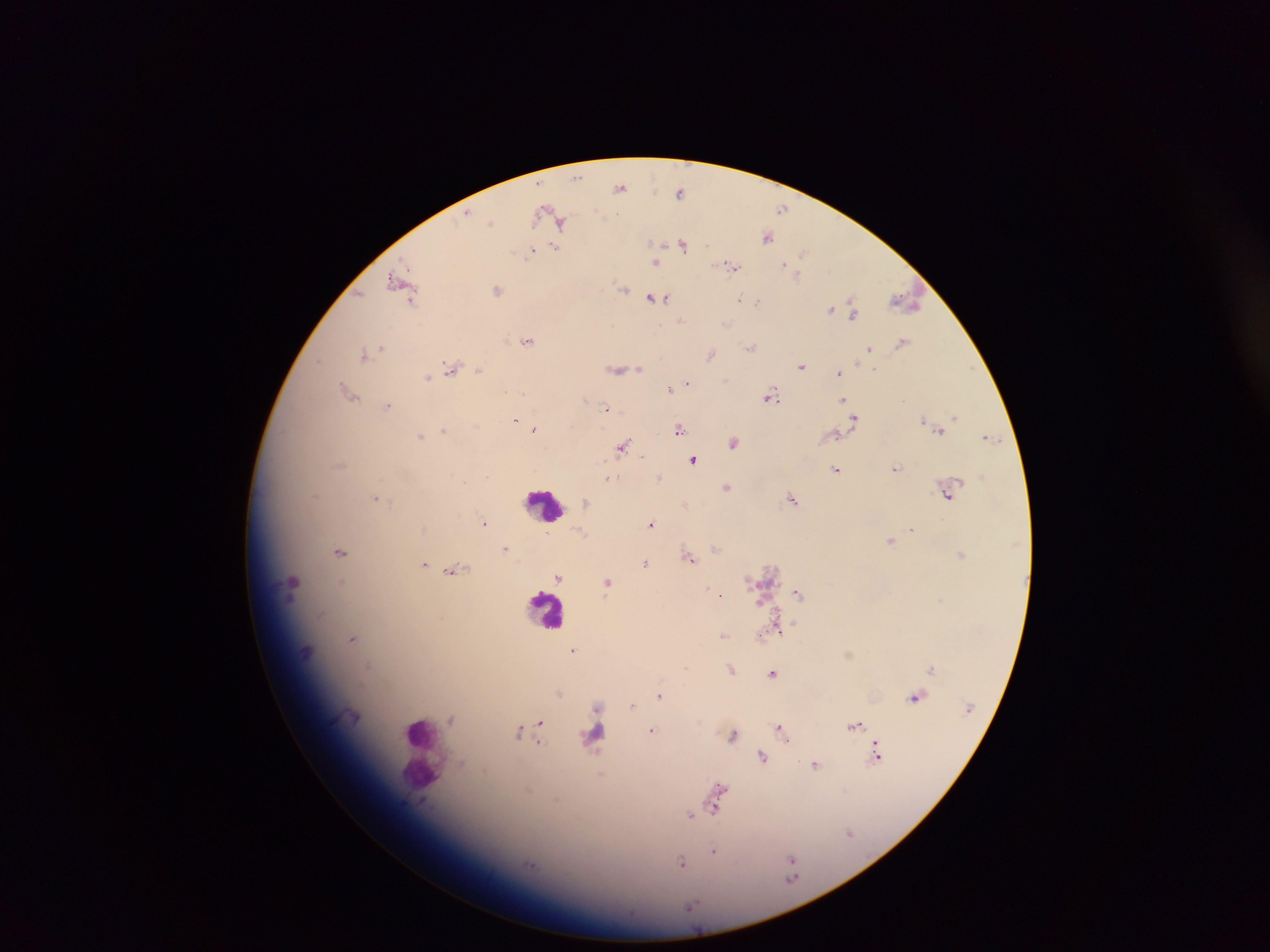

Approximate centers as [x, y] in pixels.
Summary:
  - Plasmodium parasite locations: [578, 177], [620, 187], [680, 192], [782, 209], [545, 211], [466, 215], [491, 222], [561, 222], [767, 236], [683, 245], [538, 248], [555, 249], [532, 250], [804, 252], [656, 262], [786, 264], [731, 267], [797, 274], [396, 280], [624, 288], [498, 290], [361, 294], [653, 297], [663, 298], [740, 299], [411, 301], [746, 301], [758, 301], [906, 301], [831, 309], [852, 311], [680, 320], [726, 324], [527, 341], [902, 342], [750, 346], [380, 347], [375, 350], [869, 350], [364, 354], [711, 354], [318, 361], [801, 366], [451, 367], [618, 369], [640, 369], [479, 370], [839, 372], [428, 378], [688, 383], [669, 389], [349, 392], [770, 396], [586, 399], [843, 399], [388, 405], [606, 408], [954, 416], [855, 418], [515, 420], [923, 420], [476, 424], [534, 428], [679, 428], [444, 429], [939, 431], [835, 435], [420, 436], [987, 437], [733, 441], [623, 446], [642, 456], [693, 459], [836, 469], [896, 469], [611, 478], [659, 478], [727, 487], [316, 494], [949, 495], [375, 498], [791, 499], [586, 502], [484, 523], [652, 524], [912, 529], [580, 531], [547, 535], [890, 540], [505, 549], [715, 549], [340, 552], [961, 554], [691, 559], [645, 563], [424, 564], [451, 571], [558, 576], [608, 582], [292, 583], [341, 583], [707, 587], [714, 591], [798, 593], [721, 594], [760, 602], [779, 627], [722, 636], [760, 636], [352, 639], [574, 650], [931, 668], [731, 669], [773, 673], [560, 694], [660, 696], [915, 697], [632, 705], [597, 707], [451, 720], [540, 723], [854, 725], [651, 730], [782, 731], [519, 732], [539, 733], [733, 736], [594, 737], [877, 755], [762, 757], [816, 765], [718, 790], [716, 809], [691, 815], [849, 833], [713, 851], [792, 860], [681, 862], [692, 907]
  - Leukocyte locations: [544, 504], [546, 607], [420, 743]
  - Capture: mobile-phone photograph through a microscope
  - Preparation: thick blood smear
  - Image size: 1270×952 pixels
  - Country: Ghana
  - Field of view: single